Classify this cell by malaria status.
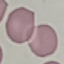

It is uninfected.

stain = Giemsa
capture = smartphone through the microscope eyepiece
preparation = thin blood smear
image type = cell patch, automatically extracted from a larger field of view and resized to 64 × 64 pixels